Assess the morphology of the red blood cells.
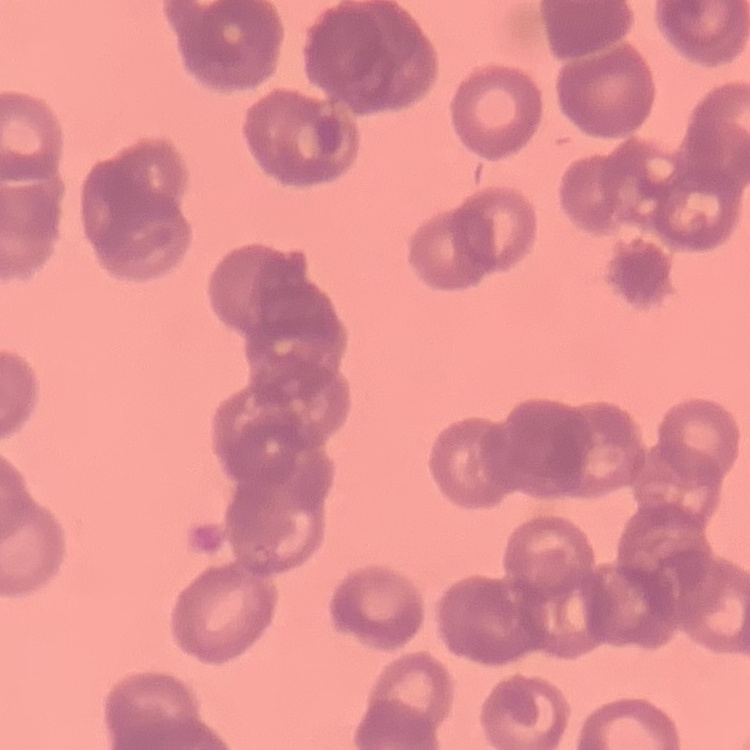

Rouleaux formation.

Summary:
  - Image type: square crop of a larger photomicrograph
  - Preparation: thin blood smear
  - Stain: Field's or Giemsa